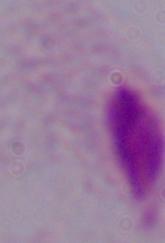
Photomicrograph. Captured at 1000x magnification. A trichomonad is shown.